Give the extent of all uninfected red blood cells.
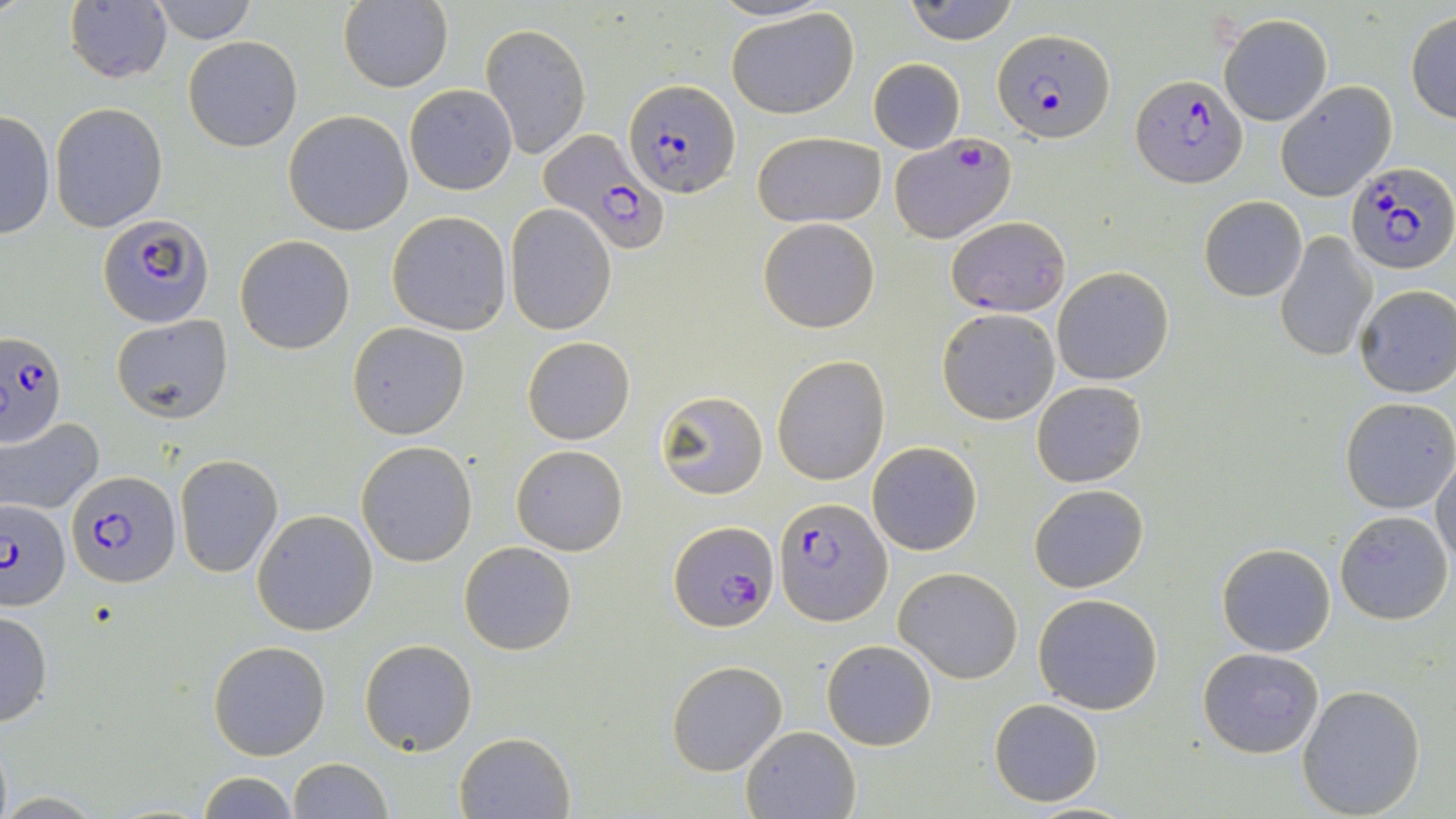

Approximate bounding boxes as [x1, y1, x2, y2] in pixels.
Uninfected red blood cells: [146, 0, 258, 44], [709, 0, 834, 24], [904, 0, 1019, 45], [64, 2, 172, 85], [337, 2, 453, 93], [726, 7, 860, 118], [1405, 12, 1455, 123], [1219, 13, 1332, 126], [481, 23, 590, 159], [183, 36, 302, 151], [868, 58, 965, 153], [1275, 81, 1396, 200], [403, 83, 516, 196], [49, 100, 167, 232], [0, 110, 55, 241], [284, 110, 414, 236], [752, 130, 886, 228], [1200, 195, 1307, 301], [505, 204, 615, 333], [385, 211, 512, 336], [758, 218, 880, 333], [1276, 231, 1376, 362], [235, 234, 355, 354], [1052, 267, 1174, 386], [1354, 285, 1456, 397], [937, 309, 1060, 424], [110, 315, 234, 422], [346, 322, 470, 439], [522, 336, 634, 445], [772, 355, 891, 485], [1031, 381, 1146, 488], [655, 389, 769, 500], [1339, 398, 1455, 515], [1, 418, 104, 516], [358, 441, 477, 567], [867, 442, 981, 556], [511, 445, 627, 556], [1432, 455, 1456, 570], [175, 456, 282, 577], [1028, 485, 1148, 593], [1335, 509, 1452, 625], [252, 510, 379, 636], [1222, 521, 1453, 635], [458, 541, 577, 656], [1216, 542, 1336, 657], [894, 567, 1022, 683], [1032, 593, 1164, 715], [0, 608, 52, 728], [359, 639, 478, 755], [822, 639, 937, 750], [209, 640, 330, 759], [1198, 647, 1325, 758], [665, 660, 788, 775], [1297, 683, 1426, 817], [989, 699, 1105, 805], [740, 725, 861, 818], [455, 731, 576, 819], [287, 757, 393, 818], [197, 769, 301, 819].

slide_level_diagnosis: Plasmodium falciparum
stain: May-Grünwald-Giemsa
modality: light microscopy
magnification: 1000x
preparation: thin blood smear
field_of_view: single
plasmodium_falciparum_infected_red_blood_cell_locations: 'approximate bounding boxes as [x1, y1, x2, y2] in pixels: [992, 28, 1117, 143], [1131, 75, 1246, 187], [623, 78, 739, 199], [535, 129, 668, 254], [888, 132, 1017, 244], [1344, 164, 1453, 275], [99, 214, 213, 327], [947, 217, 1071, 317], [0, 332, 67, 448], [65, 473, 178, 587], [0, 497, 72, 611], [776, 498, 892, 626], [668, 520, 777, 632]'
image_size: 1456×819 pixels